State which cell type is depicted.
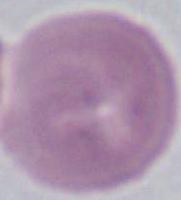
An erythrocyte.

magnification: 1000x
modality: micrograph